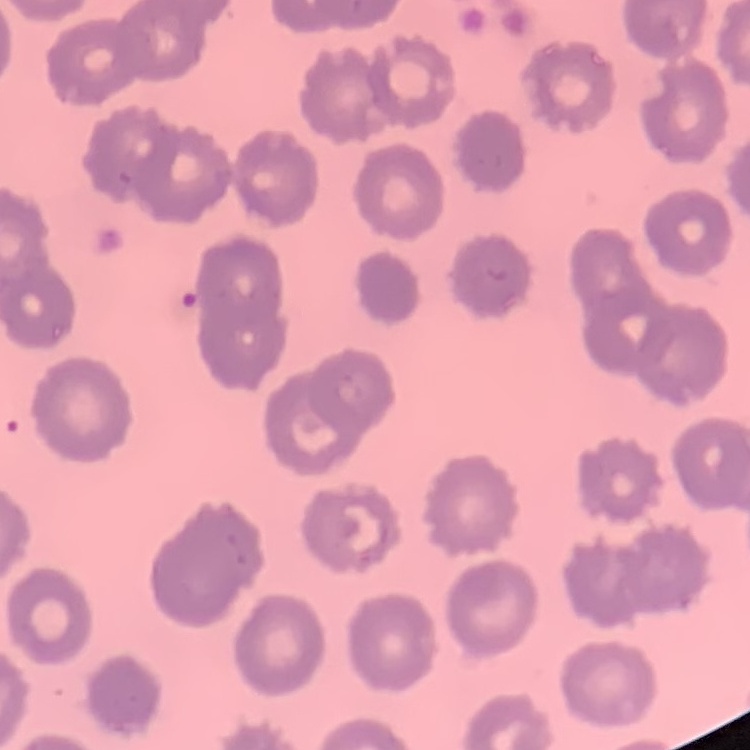
erythrocyte morphology = no rouleaux formation
stain = Field's or Giemsa
image type = one tile cut from a larger photomicrograph
preparation = thin blood film